Describe the morphology of the red blood cells.
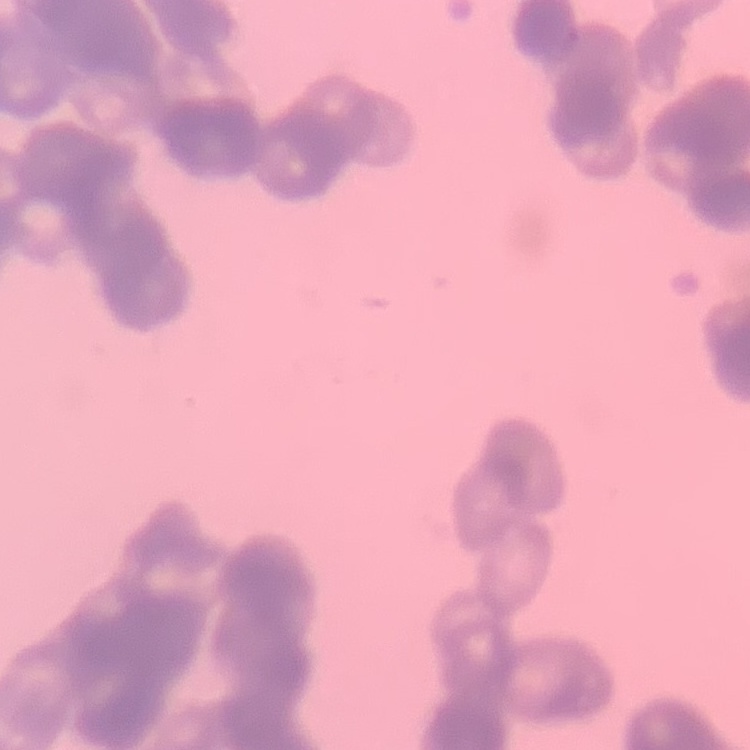

Rouleaux formation.

Summary:
  - Stain: Field's or Giemsa
  - Image type: one tile cut from a larger photomicrograph
  - Preparation: thin blood film